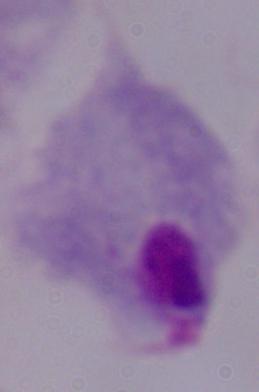

Summary:
  - Magnification: 1000x
  - Modality: micrograph
  - Identification: trichomonad